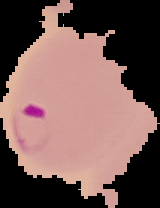 From a thin blood smear. Cell region segmented out of the field of view; the surrounding area is masked to black. Image is 160×208 pixels. Result: malaria parasites detected.